Describe the morphology of the erythrocytes.
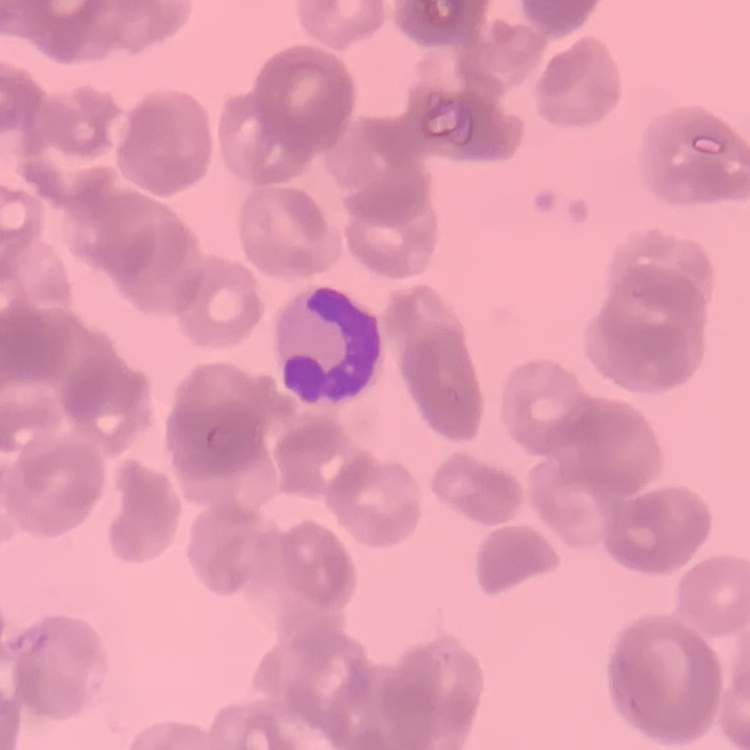
They show rouleaux formation.

Summary:
  - Stain: Field's or Giemsa
  - Image type: square crop of a larger photomicrograph
  - Preparation: thin blood film